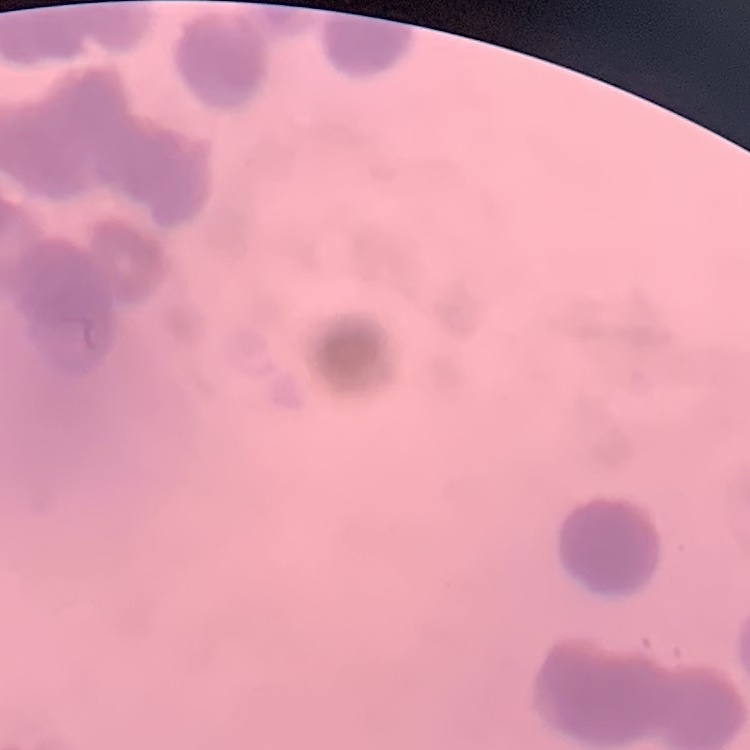
Summary:
  - Erythrocyte morphology: rouleaux formation
  - Image type: one tile cut from a larger photomicrograph
  - Stain: Field's or Giemsa
  - Preparation: thin peripheral smear